Assess this cell for malaria.
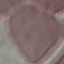

Uninfected.

Automatically extracted cell patch, resized to 64 × 64 pixels. Thin blood film. Photographed with a smartphone camera at the microscope eyepiece. Giemsa stain.